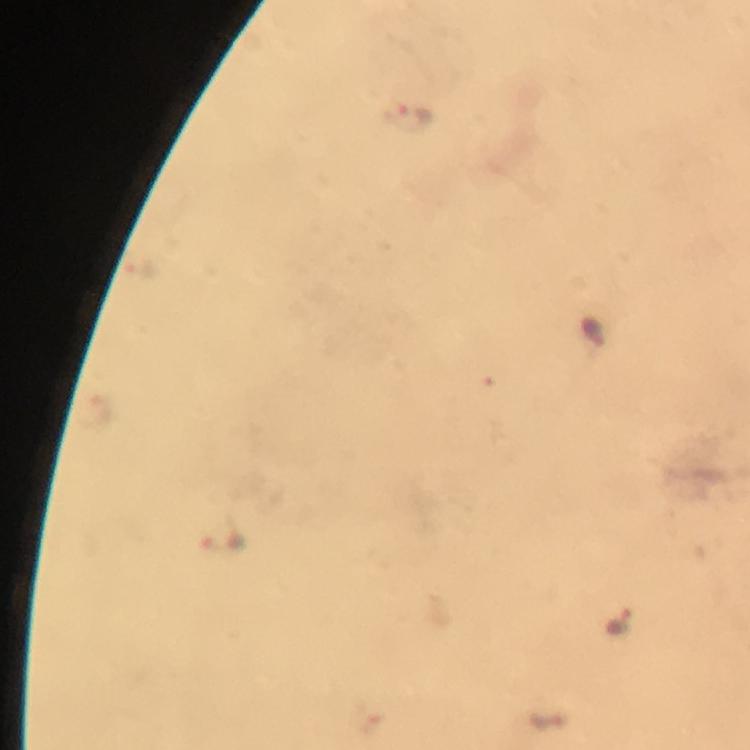
Plasmodium parasite locations = approximate centers as [x, y] in pixels: [408, 116], [139, 272], [592, 330], [222, 544], [617, 622]
image size = 750×750 pixels
immersion oil = applied
capture = smartphone mounted on the microscope
preparation = thick blood smear
cropped from = a single field of view
context = from a malaria diagnostic workup
magnification = 100x
stain = Giemsa